Locate every parasitized RBC.
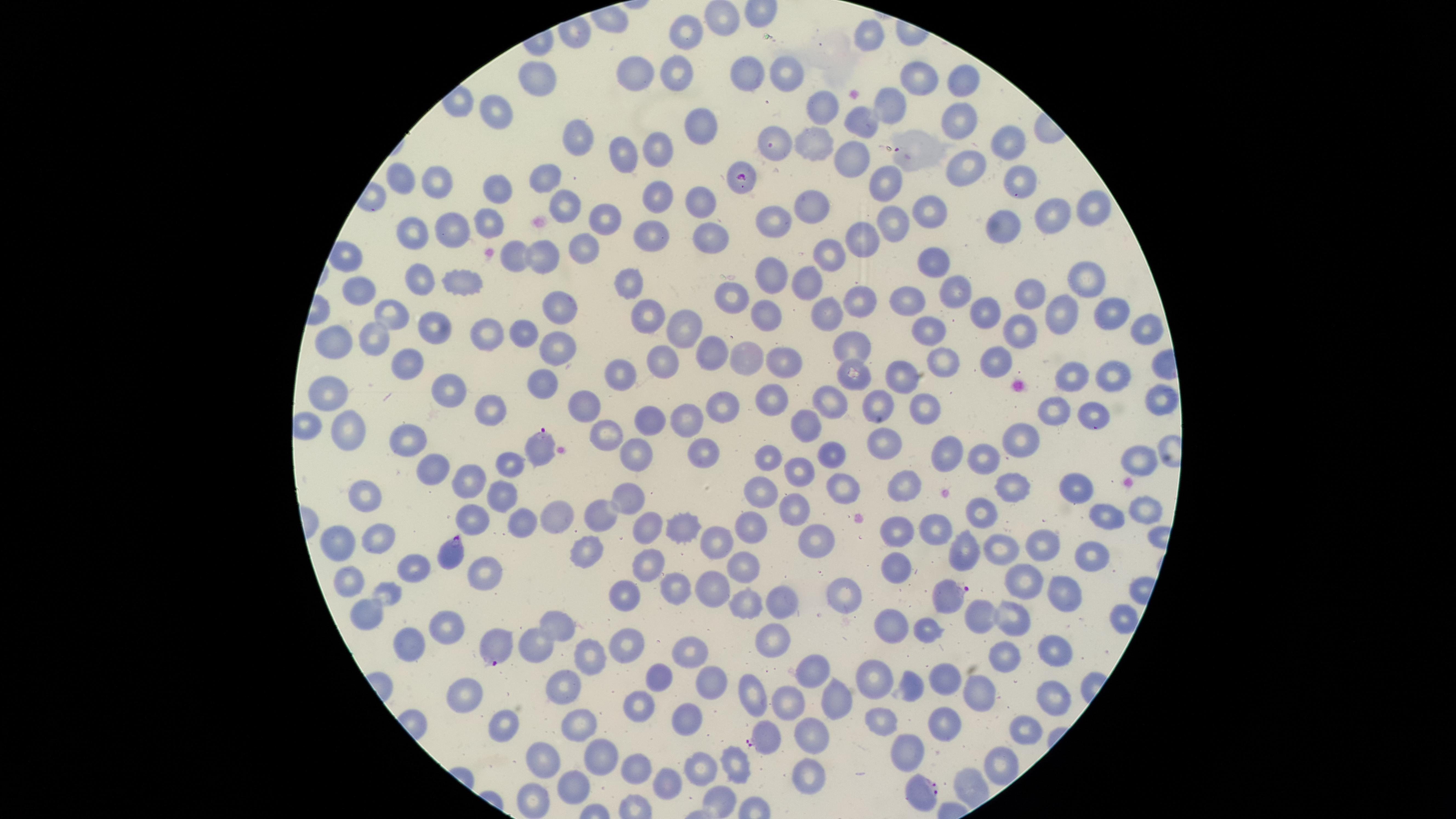
Approximate marker points as (x, y) in pixels.
Parasitized RBCs: (897, 150), (740, 178), (540, 446), (453, 554), (950, 598), (496, 646), (765, 739), (922, 794).

Approximate marker points as (x, y) in pixels. Uninfected RBCs: (721, 18), (688, 29), (866, 32), (676, 66), (749, 73), (783, 77), (916, 77), (637, 78), (534, 81), (959, 82), (888, 97), (819, 105), (498, 110), (860, 113), (952, 123), (703, 125), (573, 134), (777, 138), (1010, 146), (651, 147), (808, 147), (620, 152), (848, 153), (957, 165), (401, 178), (1018, 180), (889, 181), (435, 187), (548, 188), (493, 189), (661, 190), (701, 202), (928, 207), (1087, 207), (571, 208), (802, 211), (1051, 214), (605, 217), (893, 218), (488, 221), (770, 221), (1012, 222), (451, 225), (414, 228), (652, 232), (707, 234), (858, 236), (582, 244), (831, 246), (545, 258), (512, 259), (929, 262), (775, 275), (421, 277), (634, 277), (1090, 277), (458, 281), (357, 286), (801, 286), (1029, 290), (957, 291), (735, 295), (856, 297), (908, 300), (1108, 306), (651, 307), (830, 307), (560, 308), (984, 309), (388, 312), (1057, 313), (764, 316), (432, 326), (926, 326), (1144, 326), (685, 327), (1019, 327), (488, 333), (515, 333), (377, 338), (341, 341), (563, 343), (854, 345), (707, 351), (743, 355), (661, 358), (996, 358), (783, 361), (945, 361), (409, 362), (895, 374), (859, 376), (1068, 376), (1110, 376), (626, 377), (542, 383), (331, 387), (447, 388), (1155, 394), (829, 398), (769, 399), (877, 401), (582, 402), (926, 404), (726, 407), (490, 408), (1054, 410), (1091, 411), (649, 414), (692, 421), (807, 423), (343, 434), (611, 434), (1019, 438), (409, 441), (888, 445), (984, 450), (950, 451), (832, 452), (704, 453), (635, 455), (772, 455), (1136, 457), (433, 463), (511, 464), (801, 471), (464, 480), (899, 486), (1016, 486), (1077, 488), (845, 490), (759, 492), (497, 496), (627, 496), (363, 498), (793, 505), (978, 508), (598, 509), (1137, 509), (554, 512), (1114, 516), (471, 517), (519, 522), (754, 522), (646, 524), (934, 525), (680, 530), (894, 531), (813, 535), (377, 536), (715, 538), (338, 540), (1038, 546), (998, 549), (964, 550), (1087, 553), (594, 557), (894, 564), (641, 565), (412, 566), (738, 566), (479, 569), (348, 575), (676, 577), (712, 583), (1022, 586), (388, 590), (619, 592), (846, 593), (1063, 594), (744, 599), (780, 602), (366, 604), (1119, 616), (984, 619), (1011, 620), (445, 627), (557, 628), (892, 630), (922, 631), (408, 640), (626, 640), (771, 640), (534, 644), (1053, 647), (694, 655), (587, 656), (1006, 658), (818, 669), (874, 672), (661, 673), (711, 679), (945, 680), (909, 683), (561, 688), (980, 690), (467, 692), (751, 696), (833, 696), (1049, 697), (643, 700), (790, 701), (880, 717), (940, 717), (684, 718), (572, 719), (501, 721), (1026, 730), (815, 731), (907, 750), (546, 757), (600, 758), (998, 761), (701, 763), (731, 764), (635, 772), (809, 777), (664, 783), (571, 784), (716, 799), (534, 801). Species: Plasmodium falciparum. Thin blood film. Photographed with a smartphone camera through the microscope eyepiece. One field of view of the specimen. Giemsa stain. The visible region is circular. Image is 1456×819 pixels.